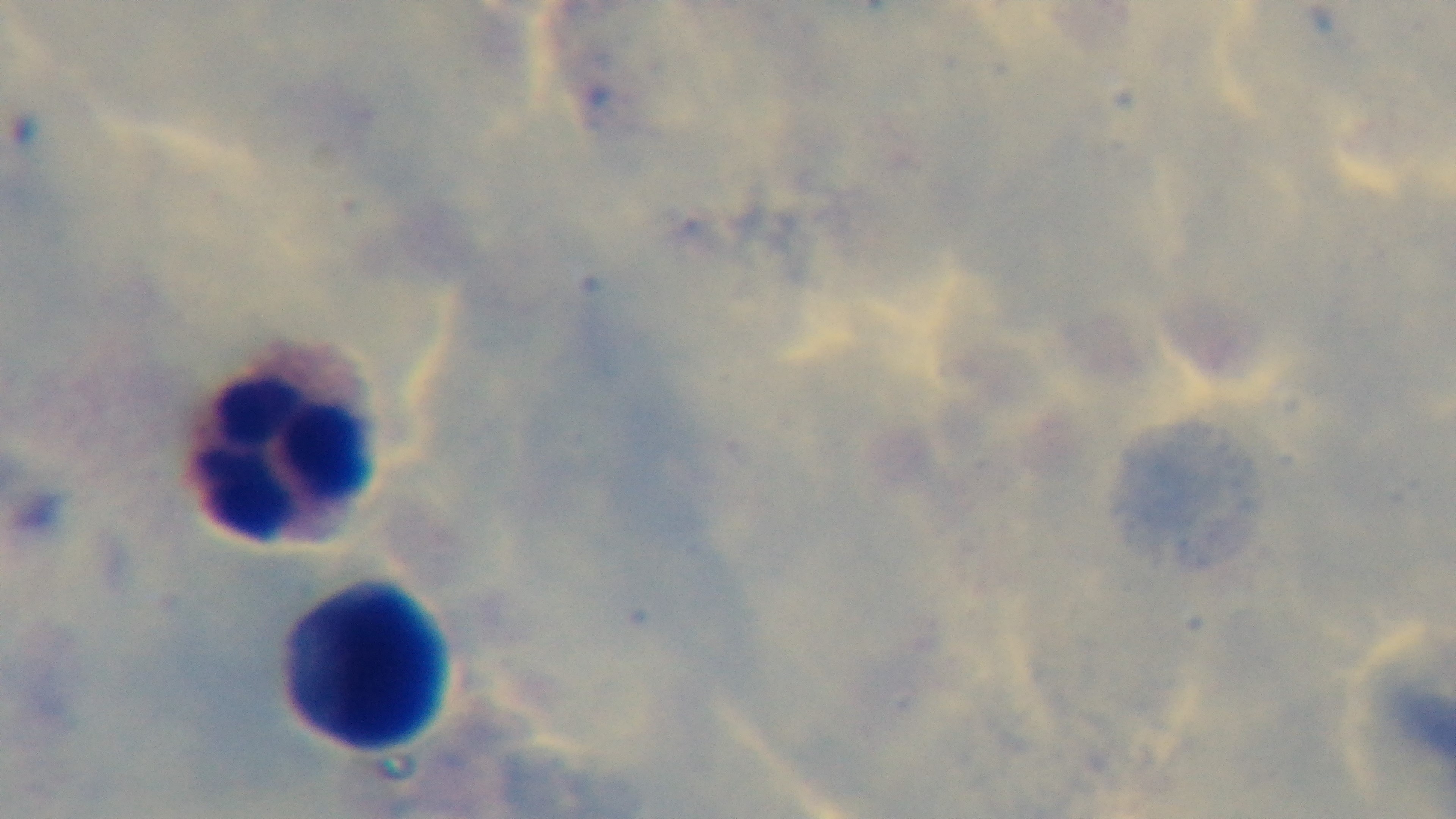

capture: mounted 4K digital camera
preparation: thick smear
field_of_view: one from the slide
modality: light microscopy
objective: 100x oil immersion
malaria_status: negative
stain: Giemsa